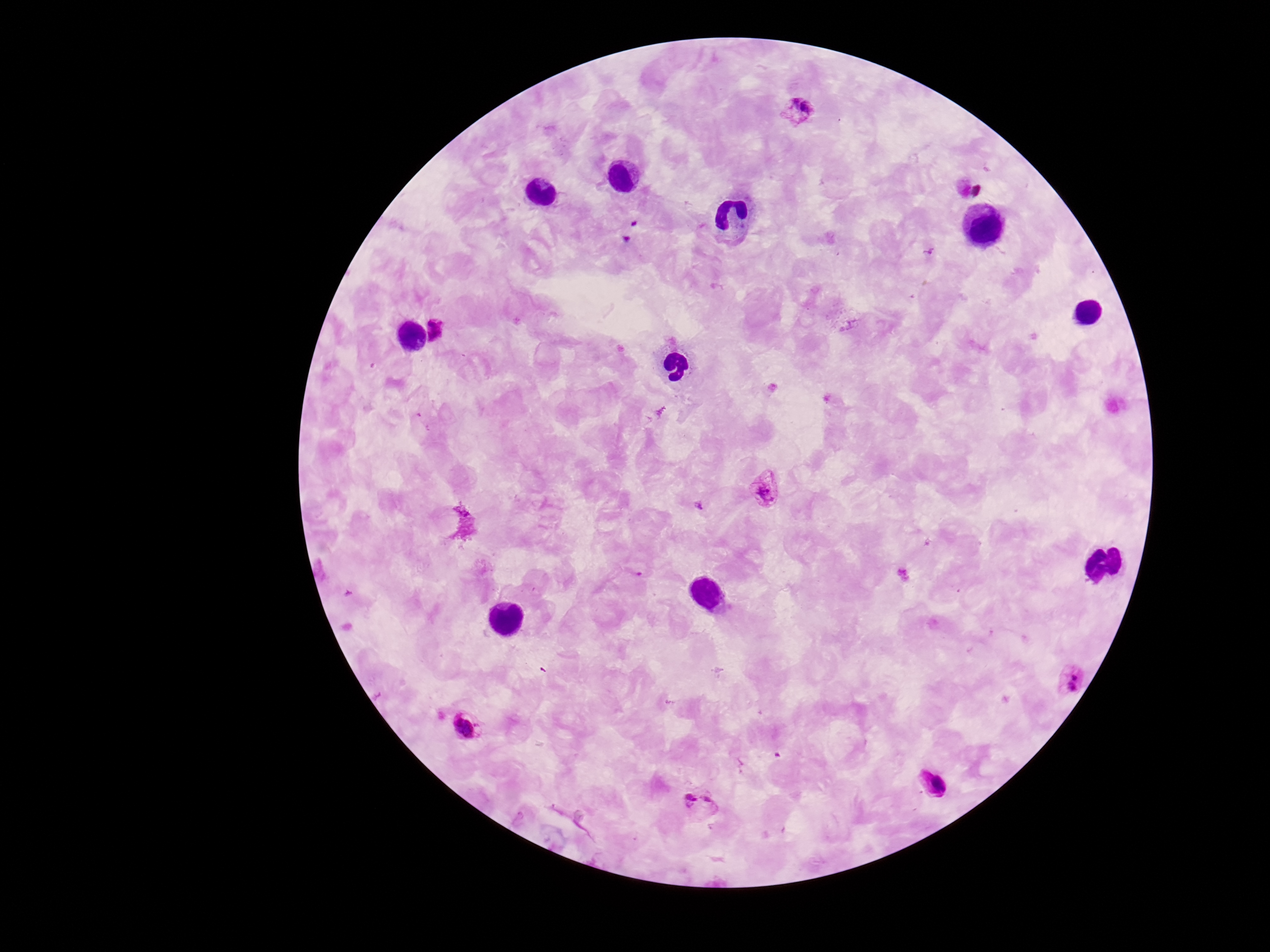
{
  "stain": "Giemsa",
  "plasmodium_parasite_locations": "approximate object centers, in pixels from the top-left corner: (x=798, y=110), (x=435, y=329), (x=764, y=490), (x=1072, y=677), (x=466, y=727), (x=933, y=784), (x=699, y=806)",
  "image_size": "1270×952 pixels",
  "preparation": "thick blood smear",
  "magnification": "100x",
  "patient_malaria_status": "positive",
  "field_of_view": "one from this slide",
  "capture": "smartphone camera through the microscope eyepiece"
}